Look for parasitized red blood cells.
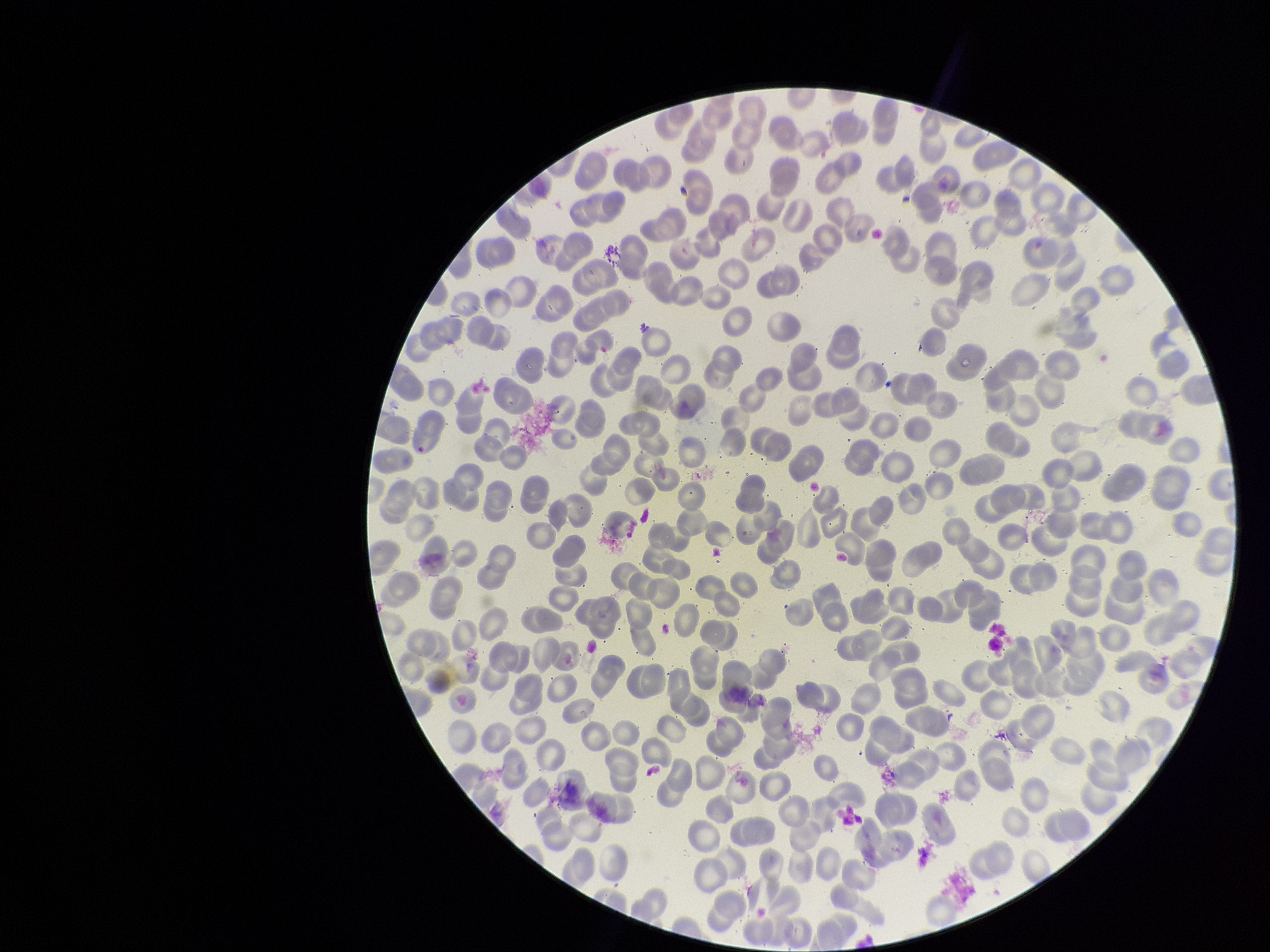
None identified.

Summary:
  - Stain: Giemsa
  - Image size: 1270×952 pixels
  - Capture: smartphone photograph through the microscope eyepiece
  - Preparation: thin
  - Field of view: single
  - Parasitized red blood cell count: 0
  - Patient malaria status: negative
  - Red blood cell count: 271